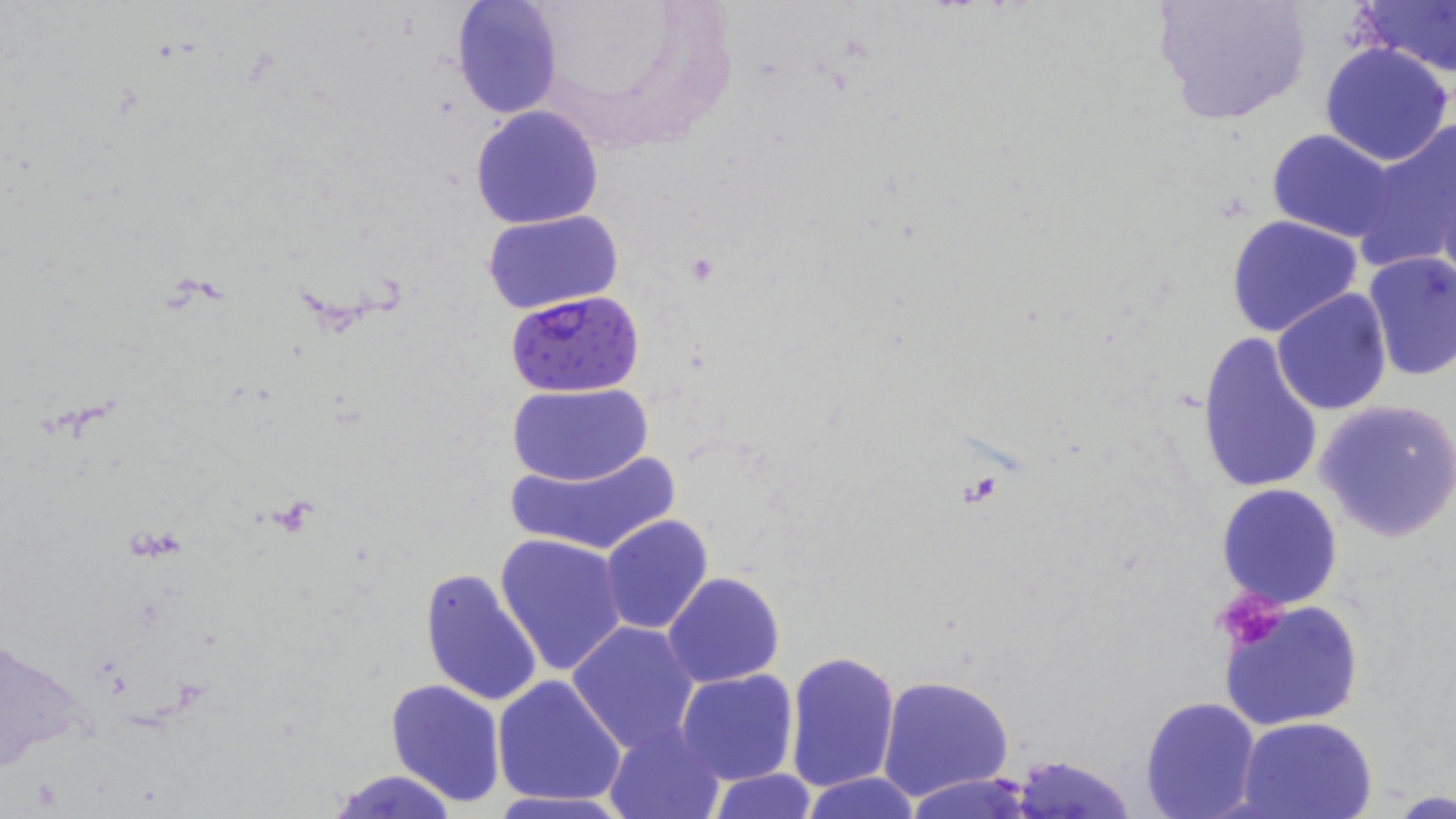
Approximate bounding boxes as (x1, y1, x2, y2) in pixels. Uninfected red blood cell locations: (1152, 0, 1312, 126), (1353, 0, 1456, 79), (450, 1, 562, 120), (1320, 43, 1454, 167), (471, 106, 604, 229), (1355, 122, 1456, 269), (1266, 129, 1399, 242), (482, 209, 627, 312), (1226, 214, 1364, 338), (1361, 252, 1455, 381), (1271, 288, 1393, 414), (1195, 330, 1324, 496), (508, 383, 654, 486), (1314, 398, 1456, 542), (498, 447, 681, 556), (1217, 484, 1343, 607), (598, 514, 714, 635), (496, 532, 629, 677), (420, 566, 543, 708), (662, 572, 785, 689), (1219, 597, 1364, 731), (567, 622, 701, 754), (0, 630, 86, 777), (784, 647, 901, 795), (676, 669, 798, 785), (875, 673, 1015, 802), (493, 674, 626, 808), (385, 677, 507, 807), (1138, 696, 1262, 819), (1237, 716, 1379, 819), (603, 723, 727, 818), (1008, 753, 1137, 819), (325, 768, 457, 819), (707, 768, 818, 819), (800, 773, 923, 819), (903, 774, 1037, 819), (1389, 787, 1452, 817). Platelet locations: (1214, 587, 1292, 652). Plasmodium falciparum-infected red blood cell locations: (506, 288, 646, 397). Slide-level diagnosis: Plasmodium falciparum. May-Grünwald-Giemsa stain. Image is 1456×819 pixels. Light microscopy. Captured at 1000x magnification. Thin blood film. One field of a larger specimen.